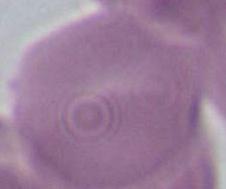
magnification = 1000x
identification = red blood cell
modality = micrograph